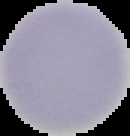

preparation: thin blood smear
image_size: 130×136 pixels
malaria_status: uninfected
image_type: cell region segmented out of the field of view; surrounding area masked to black